Report the malaria status of this cell.
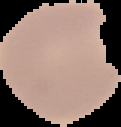

Parasitized.

Summary:
  - Preparation: thin blood film
  - Image size: 121×127 pixels
  - Image type: segmented cell region with the area outside set to black